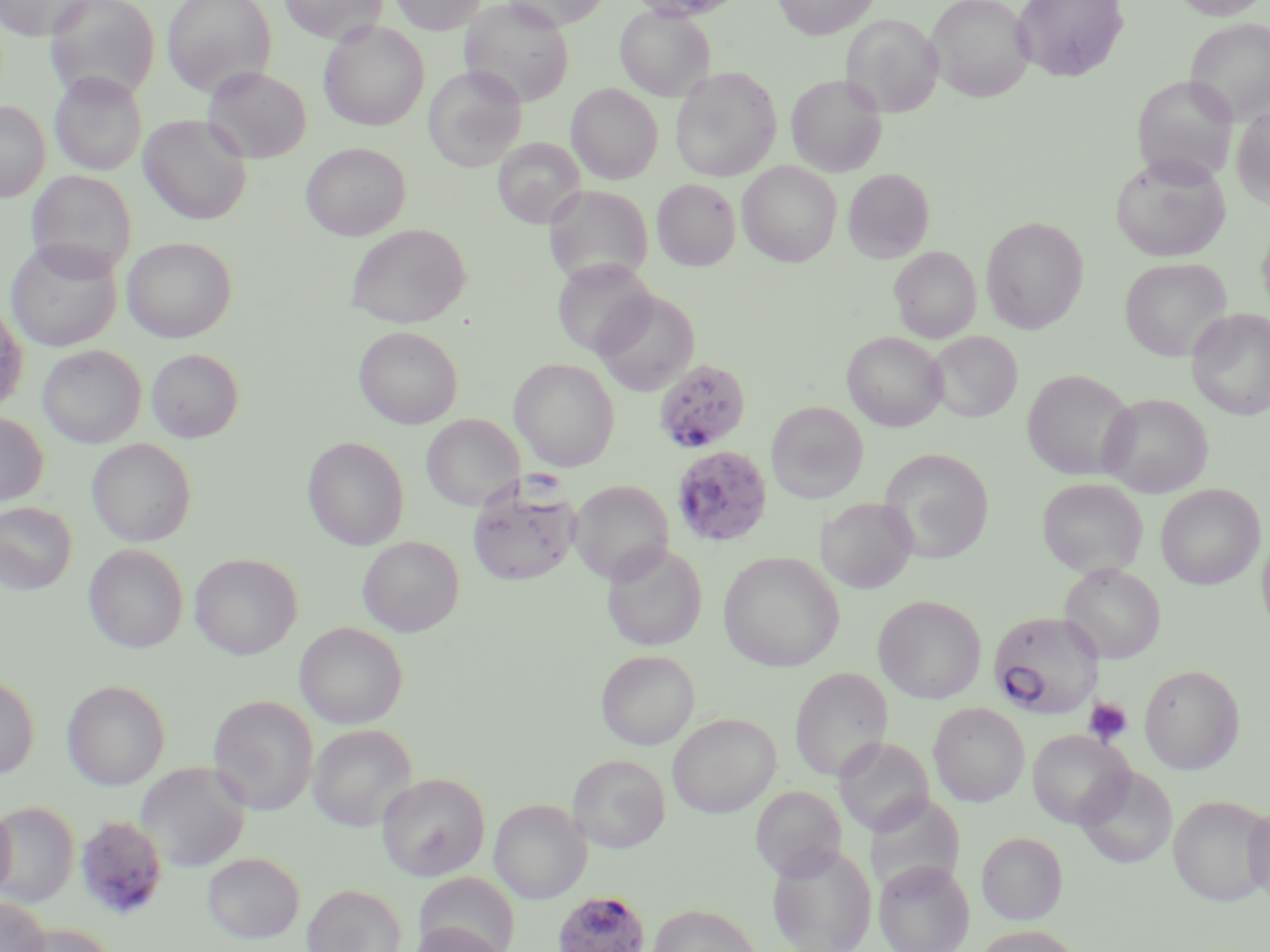

Summary:
  - Coordinate format: approximate bounding boxes as (x1,y1)-(x2,y2) corner pairs in pixels
  - Platelet locations: (1083,698)-(1133,747)
  - Uninfected red blood cell locations: (0,0)-(92,40), (43,0)-(161,103), (162,0)-(275,96), (280,0)-(387,45), (390,0)-(487,34), (459,0)-(574,106), (501,0)-(609,30), (772,0)-(879,39), (927,0)-(1035,102), (1012,0)-(1129,82), (1171,0)-(1270,20), (615,5)-(714,101), (841,13)-(943,118), (1185,18)-(1270,126), (319,21)-(429,131), (202,66)-(312,164), (424,66)-(527,171), (671,67)-(781,181), (50,72)-(147,176), (786,74)-(887,177), (1132,76)-(1239,184), (567,83)-(663,184), (0,101)-(50,202), (1231,105)-(1270,210), (139,114)-(252,225), (492,137)-(585,227), (301,143)-(410,240), (1111,154)-(1230,261), (738,162)-(841,266), (843,168)-(934,262), (27,171)-(135,279), (652,179)-(740,270), (544,185)-(653,287), (981,216)-(1088,333), (346,224)-(471,328), (1256,225)-(1270,321), (122,237)-(237,342), (6,239)-(122,352), (889,246)-(981,343), (551,258)-(656,359), (1119,258)-(1232,361), (592,289)-(700,396), (0,299)-(29,415), (1186,309)-(1270,420), (354,325)-(463,429), (843,331)-(947,431), (929,331)-(1022,423), (37,345)-(146,448), (147,349)-(243,441), (510,358)-(620,471), (1023,369)-(1136,481), (1100,394)-(1212,497), (766,401)-(868,503), (0,412)-(48,507), (421,414)-(523,512), (303,436)-(410,550), (87,439)-(196,547), (879,448)-(993,563), (1037,478)-(1147,578), (569,480)-(673,583), (1156,484)-(1264,590), (817,497)-(918,594), (0,502)-(77,595), (1257,527)-(1270,639), (358,536)-(463,636), (601,541)-(707,652), (84,544)-(188,653), (718,552)-(845,672), (190,553)-(303,660), (1059,562)-(1166,663), (874,595)-(986,704), (294,622)-(408,729), (596,650)-(699,750), (1139,664)-(1245,774), (790,668)-(891,782), (0,674)-(39,779), (62,679)-(170,790), (208,695)-(318,815), (928,703)-(1029,806), (668,713)-(780,818), (308,723)-(417,831), (1026,729)-(1132,829), (834,736)-(934,836), (567,754)-(670,853), (136,761)-(252,873), (1075,764)-(1177,868), (377,773)-(490,880), (750,785)-(846,880), (865,792)-(965,896), (1169,795)-(1269,906), (490,799)-(591,904), (0,800)-(16,901), (0,801)-(79,907), (1243,801)-(1270,905), (977,832)-(1067,925), (767,842)-(877,952), (202,852)-(305,944), (874,859)-(974,952), (413,872)-(519,951), (302,883)-(407,952), (0,895)-(50,952), (648,903)-(760,952), (407,921)-(508,952), (16,922)-(118,951), (972,925)-(1084,952)
  - Plasmodium falciparum-infected red blood cell locations: (655,358)-(751,454), (672,444)-(773,548), (467,471)-(581,586), (988,612)-(1104,718), (74,815)-(169,921), (553,889)-(650,952)
  - Slide-level diagnosis: Plasmodium falciparum
  - Field of view: one of a larger specimen
  - Modality: light microscopy
  - Magnification: 1000x
  - Preparation: thin blood film
  - Image size: 1270×952 pixels
  - Stain: May-Grünwald-Giemsa